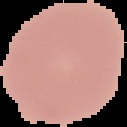 Image is 127×127 pixels. Malaria status: uninfected. Segmented cell region on a black background. From a thin blood film.